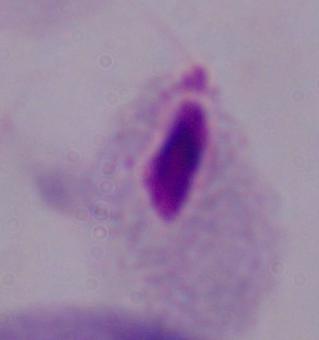

Micrograph. 1000x magnification. A trichomonad is seen.